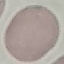

Summary:
  - Result: no malaria parasites detected
  - Preparation: thin blood smear
  - Capture: smartphone camera at the microscope eyepiece
  - Image type: cell patch, automatically extracted from a larger field of view and resized to 64 × 64 pixels
  - Stain: Giemsa